Report the malaria status of this cell.
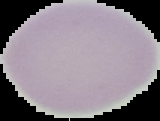

It is uninfected.

image_type: segmented cell region on a black background
image_size: 160×121 pixels
preparation: thin blood smear